Comment on the background quality.
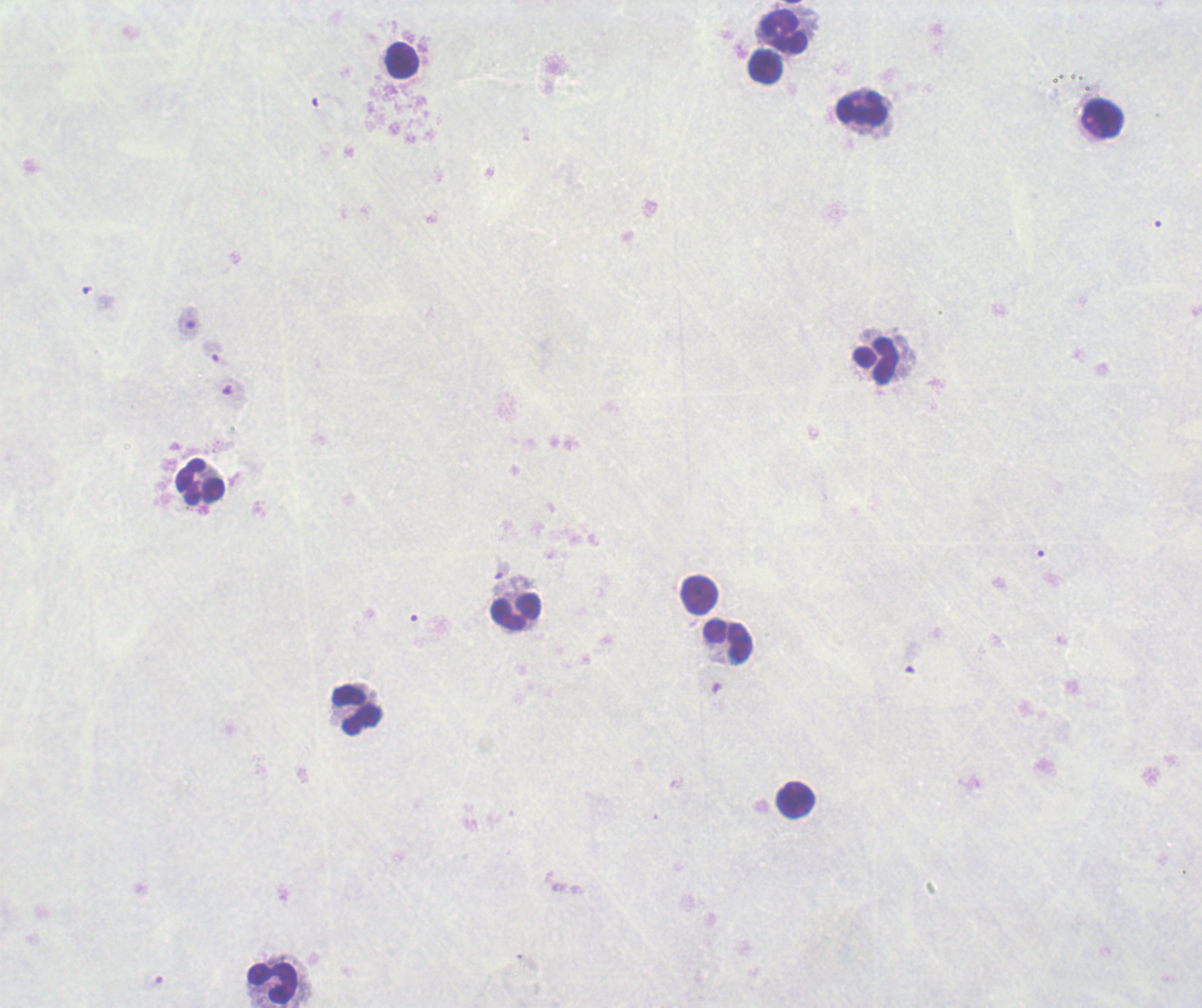

It is poor.

Approximate object centers, in pixels from the top-left corner. Leukocyte locations: (x=784, y=33), (x=403, y=61), (x=767, y=67), (x=862, y=109), (x=1103, y=119), (x=876, y=362), (x=201, y=483), (x=700, y=596), (x=517, y=612), (x=729, y=641), (x=358, y=710), (x=796, y=800), (x=273, y=983). Previously used in an actual diagnosis. Thick blood film. Romanowsky stain. One field from this slide. Captured at 100x magnification. Image is 1202×1008 pixels. Result: negative for malaria parasites.